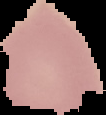
image_size: 106×115 pixels
image_type: segmented cell region with the area outside set to black
result: no malaria parasites detected
preparation: thin blood film